Report the malaria status of this cell.
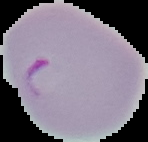

Parasitized.

image_type: segmented cell region with the area outside set to black
preparation: thin blood film
image_size: 148×142 pixels